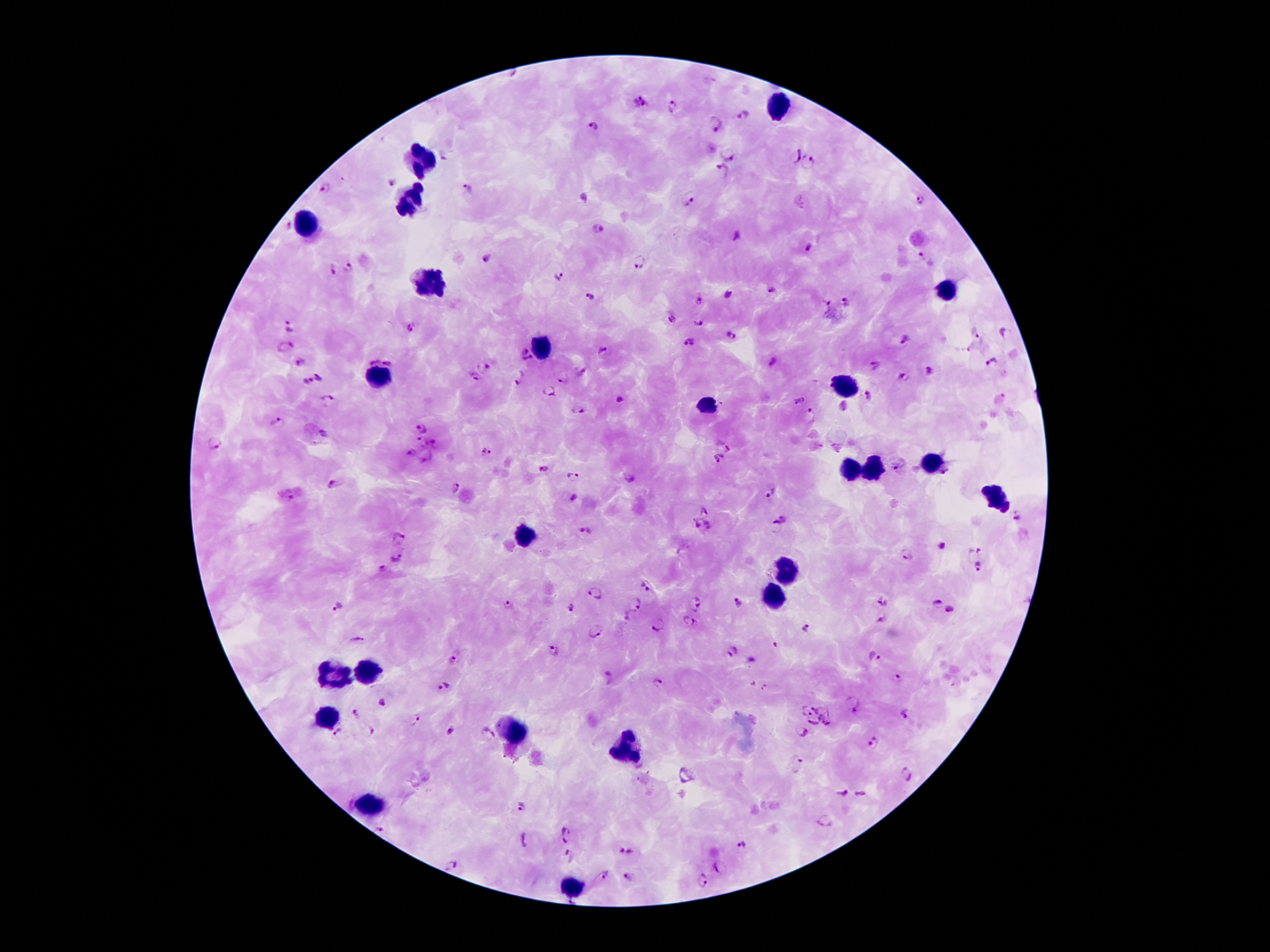
Approximate centers as [x, y] in pixels. Plasmodium parasite locations: [639, 101], [674, 107], [744, 116], [715, 124], [594, 126], [727, 155], [794, 156], [810, 163], [723, 168], [391, 183], [326, 188], [466, 190], [688, 200], [920, 200], [288, 225], [599, 227], [737, 235], [809, 247], [921, 256], [487, 257], [640, 260], [349, 267], [331, 270], [560, 275], [773, 289], [729, 294], [590, 297], [699, 299], [846, 301], [826, 306], [671, 319], [699, 322], [290, 326], [411, 328], [975, 332], [1005, 332], [732, 335], [905, 338], [688, 343], [287, 347], [523, 349], [602, 350], [371, 358], [389, 359], [528, 360], [301, 362], [773, 363], [992, 364], [486, 365], [875, 366], [930, 371], [582, 373], [319, 377], [904, 377], [476, 378], [521, 378], [563, 378], [308, 381], [548, 391], [867, 396], [328, 399], [620, 399], [799, 402], [578, 411], [810, 415], [276, 424], [422, 428], [325, 433], [215, 443], [422, 443], [724, 443], [436, 444], [485, 452], [411, 453], [427, 458], [719, 460], [544, 468], [897, 469], [948, 474], [574, 476], [631, 479], [335, 484], [452, 486], [772, 493], [572, 499], [706, 510], [1017, 516], [781, 520], [696, 524], [711, 525], [585, 532], [399, 536], [942, 546], [973, 553], [908, 554], [397, 556], [383, 567], [979, 568], [646, 586], [595, 592], [884, 599], [696, 602], [636, 603], [738, 603], [936, 604], [506, 605], [337, 606], [571, 608], [949, 609], [628, 616], [882, 621], [689, 622], [661, 624], [806, 627], [595, 631], [357, 637], [554, 650], [733, 650], [875, 656], [454, 659], [752, 661], [609, 675], [897, 678], [657, 685], [444, 686], [382, 703], [854, 703], [821, 707], [808, 711], [355, 713], [906, 714], [828, 717], [415, 719], [814, 724], [451, 730], [369, 731], [338, 732], [802, 732], [487, 733], [873, 742], [796, 762], [907, 775], [842, 792], [861, 795], [522, 806], [826, 822], [381, 830], [567, 834], [523, 840], [743, 844], [627, 852], [571, 856], [450, 865], [719, 868], [602, 876], [628, 879], [701, 881]. Leukocyte locations: [778, 106], [419, 160], [410, 201], [307, 223], [429, 282], [944, 293], [540, 349], [380, 378], [844, 384], [708, 406], [928, 463], [872, 466], [851, 470], [998, 498], [524, 535], [785, 567], [771, 599], [372, 670], [335, 674], [326, 719], [512, 730], [625, 749], [366, 809], [573, 887]. Image is 1270×952 pixels. Giemsa-stained preparation. Photographed through the microscope eyepiece with a smartphone camera. 100x magnification. Thick peripheral-blood smear. Patient malaria status: infected with Plasmodium falciparum. Single field of view.